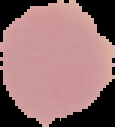

Summary:
  - Result: no malaria parasites detected
  - Image type: segmented cell region with the area outside set to black
  - Preparation: thin blood film
  - Image size: 115×127 pixels